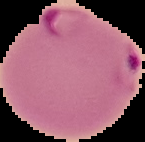
result: Plasmodium parasites detected
image_size: 145×142 pixels
image_type: cell region segmented out of the field of view; surrounding area masked to black
preparation: thin blood smear